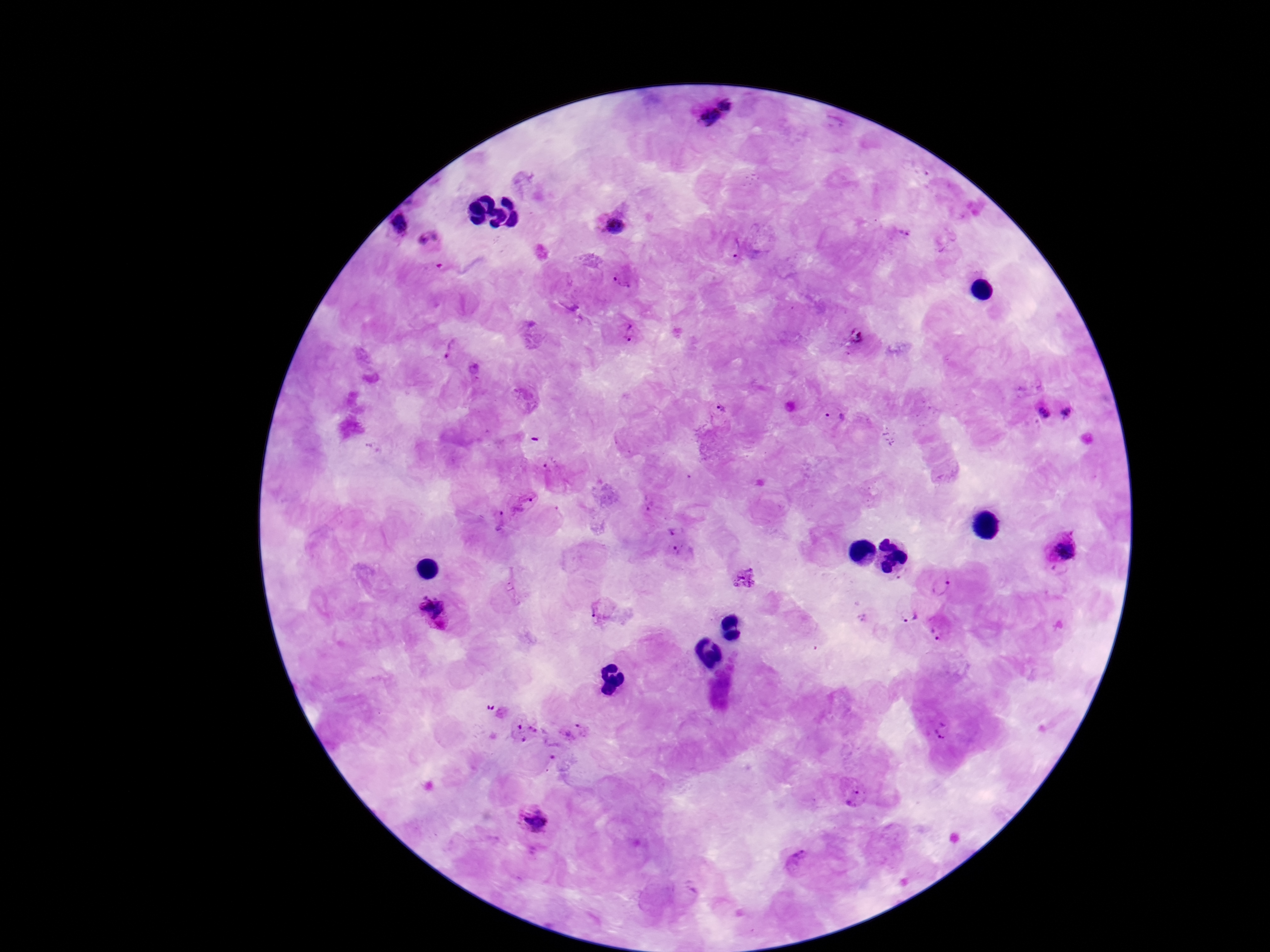
image size = 1270×952 pixels
magnification = 100x
field of view = single
preparation = thick peripheral-blood smear
Plasmodium parasite locations = approximate centers as [x, y] in pixels: [716, 115], [401, 224], [614, 225], [903, 230], [430, 240], [736, 250], [624, 278], [625, 331], [858, 340], [453, 352], [845, 357], [720, 409], [1071, 409], [835, 413], [1043, 413], [553, 467], [523, 501], [649, 503], [499, 520], [677, 529], [1061, 548], [678, 553], [742, 581], [940, 586], [599, 611], [907, 613], [435, 614], [863, 619], [941, 629], [491, 707], [526, 730], [576, 731], [942, 731], [552, 752], [855, 795], [532, 819], [801, 863]
patient malaria status = positive
stain = Giemsa
capture = smartphone camera through the microscope eyepiece